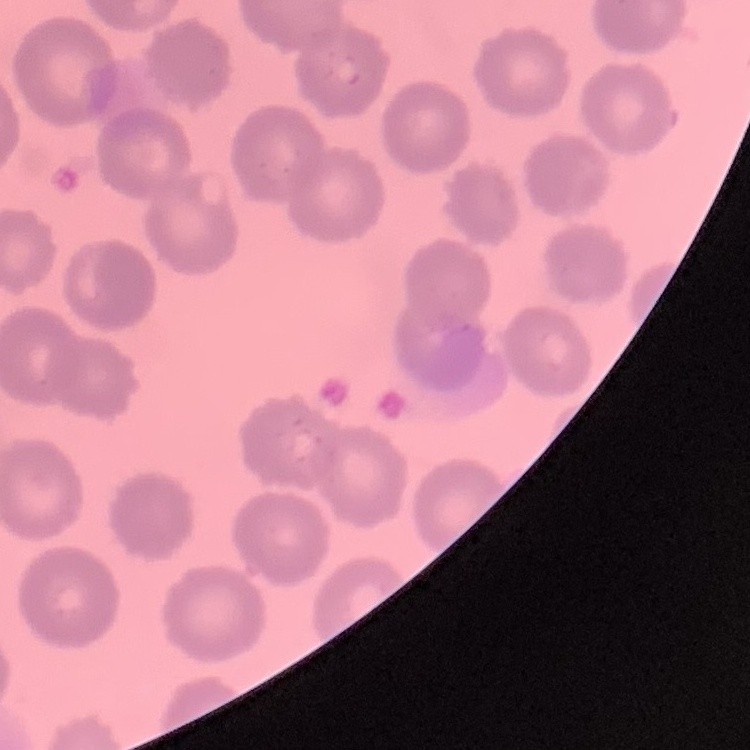
erythrocyte_morphology: no rouleaux formation
preparation: thin peripheral smear
stain: Field's or Giemsa
image_type: square crop of a larger photomicrograph